Locate every Plasmodium ovale-infected red blood cell.
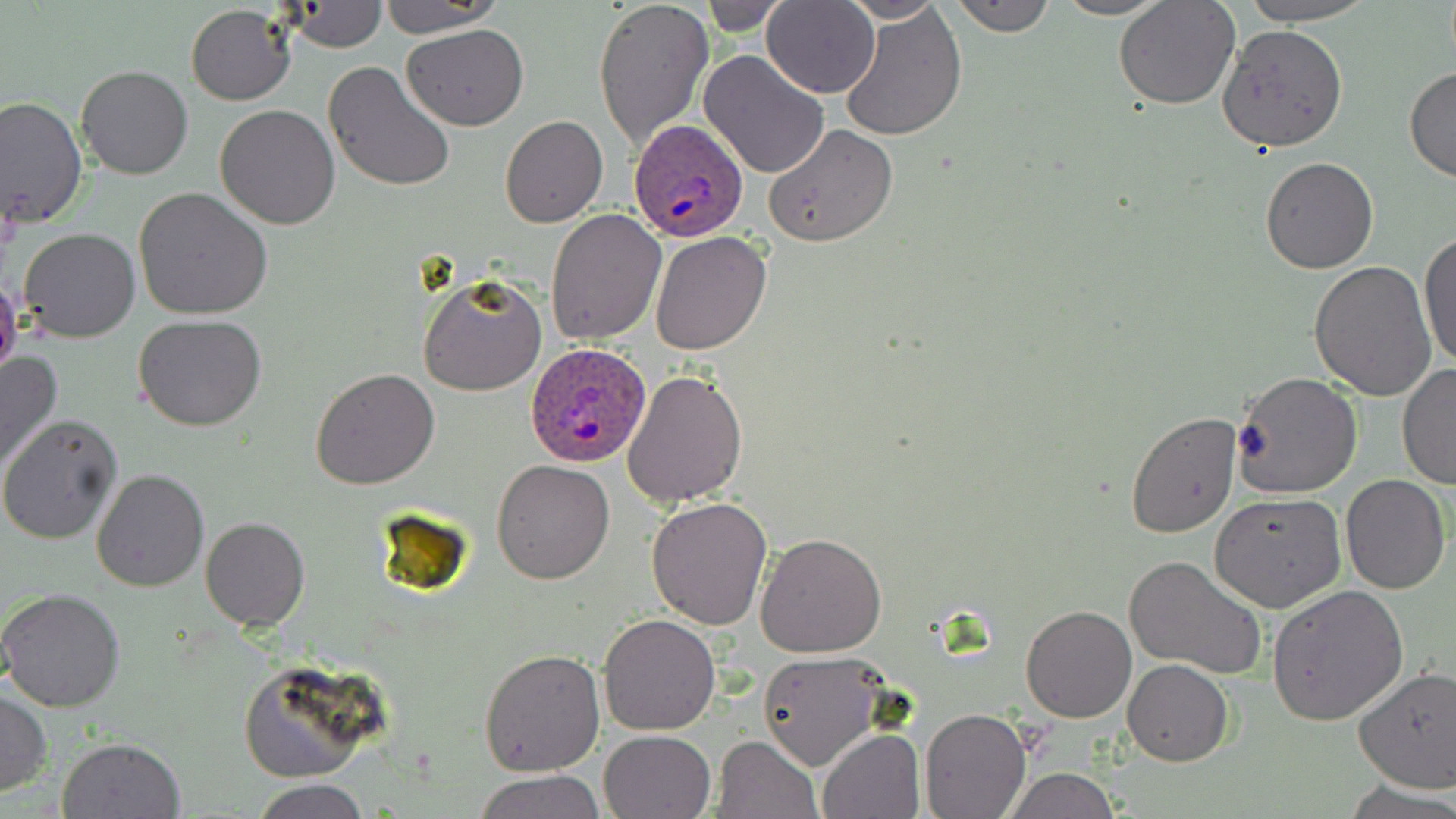

Approximate bounding boxes as named x1/y1/x2/y2 corners in pixels.
Plasmodium ovale-infected red blood cells: (x1=627, y1=120, x2=750, y2=241), (x1=527, y1=339, x2=651, y2=465).

Summary:
  - Uninfected red blood cell locations: (x1=591, y1=0, x2=711, y2=151), (x1=698, y1=0, x2=792, y2=36), (x1=840, y1=0, x2=947, y2=21), (x1=949, y1=0, x2=1056, y2=37), (x1=1052, y1=0, x2=1170, y2=19), (x1=1235, y1=0, x2=1374, y2=24), (x1=762, y1=1, x2=881, y2=98), (x1=1114, y1=1, x2=1238, y2=109), (x1=286, y1=2, x2=388, y2=53), (x1=378, y1=2, x2=502, y2=35), (x1=839, y1=4, x2=966, y2=140), (x1=186, y1=5, x2=296, y2=105), (x1=1218, y1=24, x2=1350, y2=152), (x1=403, y1=25, x2=528, y2=128), (x1=698, y1=48, x2=831, y2=179), (x1=323, y1=63, x2=456, y2=192), (x1=77, y1=65, x2=193, y2=181), (x1=1404, y1=65, x2=1456, y2=183), (x1=0, y1=95, x2=88, y2=229), (x1=215, y1=104, x2=342, y2=229), (x1=499, y1=114, x2=608, y2=228), (x1=763, y1=124, x2=897, y2=247), (x1=1260, y1=157, x2=1378, y2=273), (x1=134, y1=186, x2=275, y2=319), (x1=543, y1=209, x2=667, y2=345), (x1=18, y1=228, x2=141, y2=343), (x1=1418, y1=229, x2=1456, y2=375), (x1=650, y1=230, x2=772, y2=354), (x1=1309, y1=261, x2=1438, y2=400), (x1=418, y1=273, x2=547, y2=394), (x1=0, y1=274, x2=23, y2=382), (x1=133, y1=315, x2=267, y2=431), (x1=0, y1=348, x2=62, y2=475), (x1=1397, y1=361, x2=1456, y2=490), (x1=311, y1=369, x2=439, y2=489), (x1=621, y1=369, x2=748, y2=509), (x1=1231, y1=372, x2=1364, y2=498), (x1=1125, y1=412, x2=1242, y2=539), (x1=0, y1=416, x2=122, y2=544), (x1=493, y1=461, x2=616, y2=584), (x1=92, y1=467, x2=209, y2=593), (x1=1341, y1=475, x2=1449, y2=593), (x1=1210, y1=492, x2=1347, y2=612), (x1=646, y1=496, x2=774, y2=630), (x1=200, y1=517, x2=310, y2=631), (x1=755, y1=531, x2=887, y2=659), (x1=1123, y1=554, x2=1268, y2=679), (x1=1266, y1=584, x2=1408, y2=725), (x1=1, y1=588, x2=126, y2=712), (x1=1020, y1=605, x2=1137, y2=722), (x1=598, y1=612, x2=721, y2=735), (x1=478, y1=648, x2=604, y2=777), (x1=757, y1=652, x2=889, y2=770), (x1=1124, y1=660, x2=1234, y2=766), (x1=1354, y1=666, x2=1456, y2=792), (x1=0, y1=691, x2=50, y2=796), (x1=920, y1=707, x2=1031, y2=818), (x1=600, y1=729, x2=716, y2=819), (x1=816, y1=729, x2=925, y2=818), (x1=715, y1=735, x2=822, y2=819), (x1=57, y1=737, x2=186, y2=818), (x1=1001, y1=768, x2=1123, y2=818), (x1=474, y1=769, x2=604, y2=819), (x1=250, y1=778, x2=373, y2=818), (x1=1343, y1=778, x2=1456, y2=819)
  - Slide-level diagnosis: Plasmodium ovale
  - Modality: optical microscopy
  - Image size: 1456×819 pixels
  - Preparation: thin blood smear
  - Field of view: single
  - Stain: May-Grünwald-Giemsa
  - Magnification: 1000x